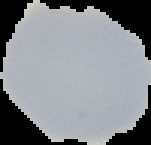

Summary:
  - Malaria status: uninfected
  - Image type: cell region segmented out of the field of view; surrounding area masked to black
  - Preparation: thin blood smear
  - Image size: 151×145 pixels